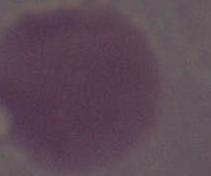
Summary:
  - Magnification: 1000x
  - Modality: micrograph
  - Identification: red blood cell